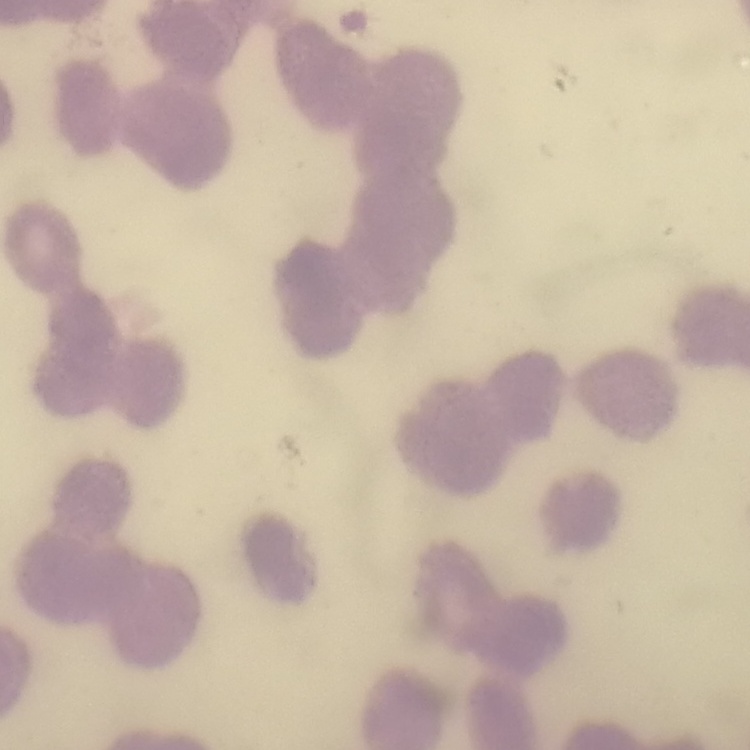

The red blood cells show rouleaux formation. Stained with either Field's or Giemsa. Thin blood smear. One tile cut from a larger photomicrograph.